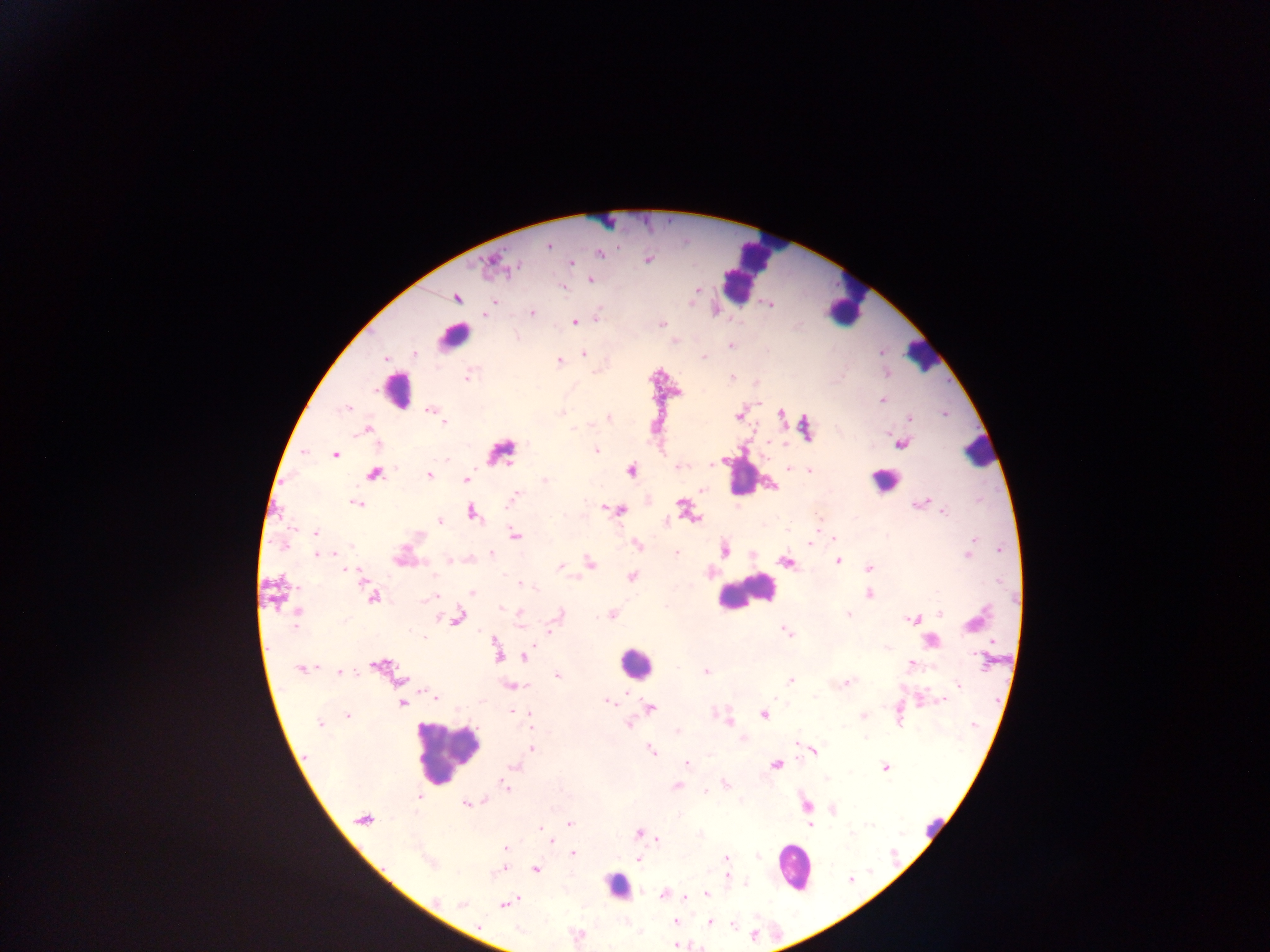

Approximate centers as x y in pixels.
Summary:
  - Malaria parasite locations: 548 246; 600 254; 648 260; 572 263; 490 264; 517 267; 590 279; 563 287; 695 291; 457 298; 494 301; 532 313; 485 315; 598 318; 575 322; 662 324; 730 346; 415 354; 584 354; 704 356; 385 358; 559 362; 468 377; 732 377; 882 399; 346 408; 430 409; 561 413; 738 414; 782 414; 944 414; 608 418; 909 419; 444 422; 369 429; 574 430; 769 443; 901 444; 597 450; 305 452; 503 452; 335 455; 712 465; 679 467; 789 468; 631 470; 809 471; 375 473; 429 475; 466 479; 545 480; 773 486; 703 491; 516 496; 357 504; 920 504; 681 505; 620 510; 472 512; 944 512; 690 517; 440 521; 817 527; 316 532; 515 535; 834 538; 973 540; 637 545; 809 545; 282 546; 971 547; 999 549; 726 551; 676 553; 491 554; 317 555; 968 555; 449 561; 837 561; 590 562; 786 562; 560 566; 869 568; 346 569; 349 570; 632 576; 363 580; 522 584; 534 587; 472 593; 869 593; 431 597; 373 598; 502 608; 297 611; 520 613; 941 613; 848 614; 558 615; 612 615; 458 618; 912 619; 555 621; 974 622; 519 625; 551 630; 787 631; 423 636; 496 642; 931 642; 887 648; 498 656; 976 656; 524 657; 983 660; 911 664; 377 666; 300 669; 706 672; 341 673; 557 675; 402 679; 790 681; 847 683; 958 685; 513 686; 626 692; 430 695; 434 697; 815 697; 943 700; 608 701; 401 704; 651 707; 512 712; 527 713; 764 714; 863 715; 348 716; 728 721; 319 723; 628 723; 973 725; 678 732; 742 738; 866 738; 531 748; 650 750; 814 750; 687 763; 776 765; 514 767; 885 767; 826 779; 726 783; 677 786; 506 787; 706 792; 419 797; 482 800; 466 803; 806 804; 833 809; 363 819; 569 824; 810 826; 542 829; 638 834; 852 834; 657 839; 551 840; 506 849; 573 853; 757 857; 726 858; 638 860; 428 863; 536 869; 498 870; 727 875; 850 879; 745 884; 663 894; 706 894; 686 898; 462 904; 505 905; 676 921; 709 922; 734 926; 675 945
  - Leukocyte locations: 754 264; 845 299; 454 337; 921 355; 397 391; 979 452; 741 474; 883 480; 745 592; 634 663; 447 751; 932 825; 793 867; 617 885
  - Capture: mobile-phone photograph through a microscope
  - Country: Ghana
  - Field of view: single
  - Preparation: thick blood film
  - Image size: 1270×952 pixels